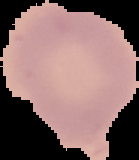
From a thin blood smear. Image is 139×160 pixels. Result: no Plasmodium parasites detected. Segmented cell region on a black background.